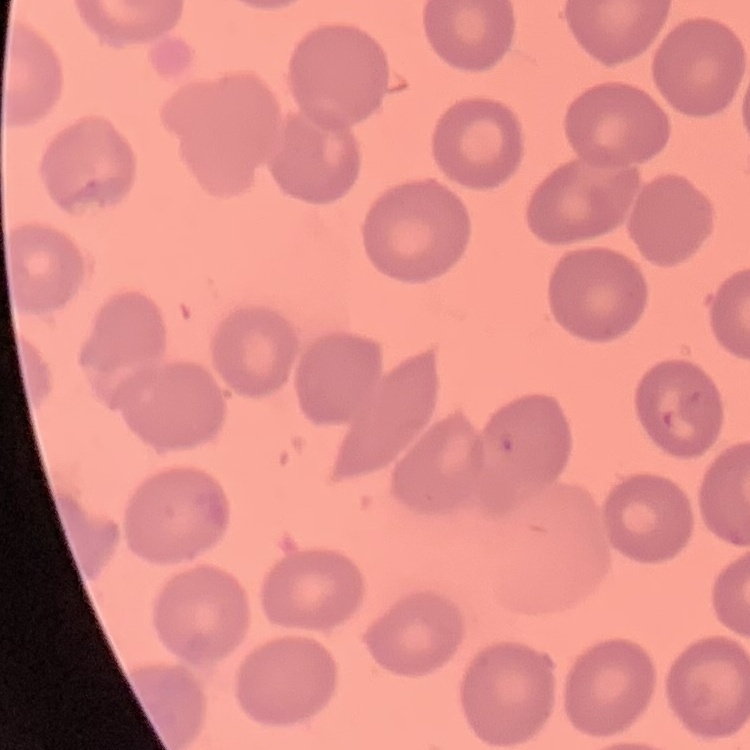
Summary:
  - Red blood cell morphology: no rouleaux formation
  - Stain: Field's or Giemsa
  - Image type: square crop of a larger photomicrograph
  - Preparation: thin blood film